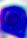

{
  "magnification": "400x",
  "modality": "photomicrograph",
  "identification": "white blood cell"
}